Assess this cell for malaria.
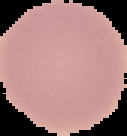
Uninfected.

Image is 127×136 pixels. Cell region segmented out of the field of view; the surrounding area is masked to black. From a thin blood smear.